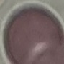
Summary:
  - Malaria status: uninfected
  - Preparation: thin blood smear
  - Image type: automatically extracted cell patch, resized to 64 × 64 pixels
  - Capture: smartphone camera at the microscope eyepiece
  - Stain: Giemsa